Look for Plasmodium parasites.
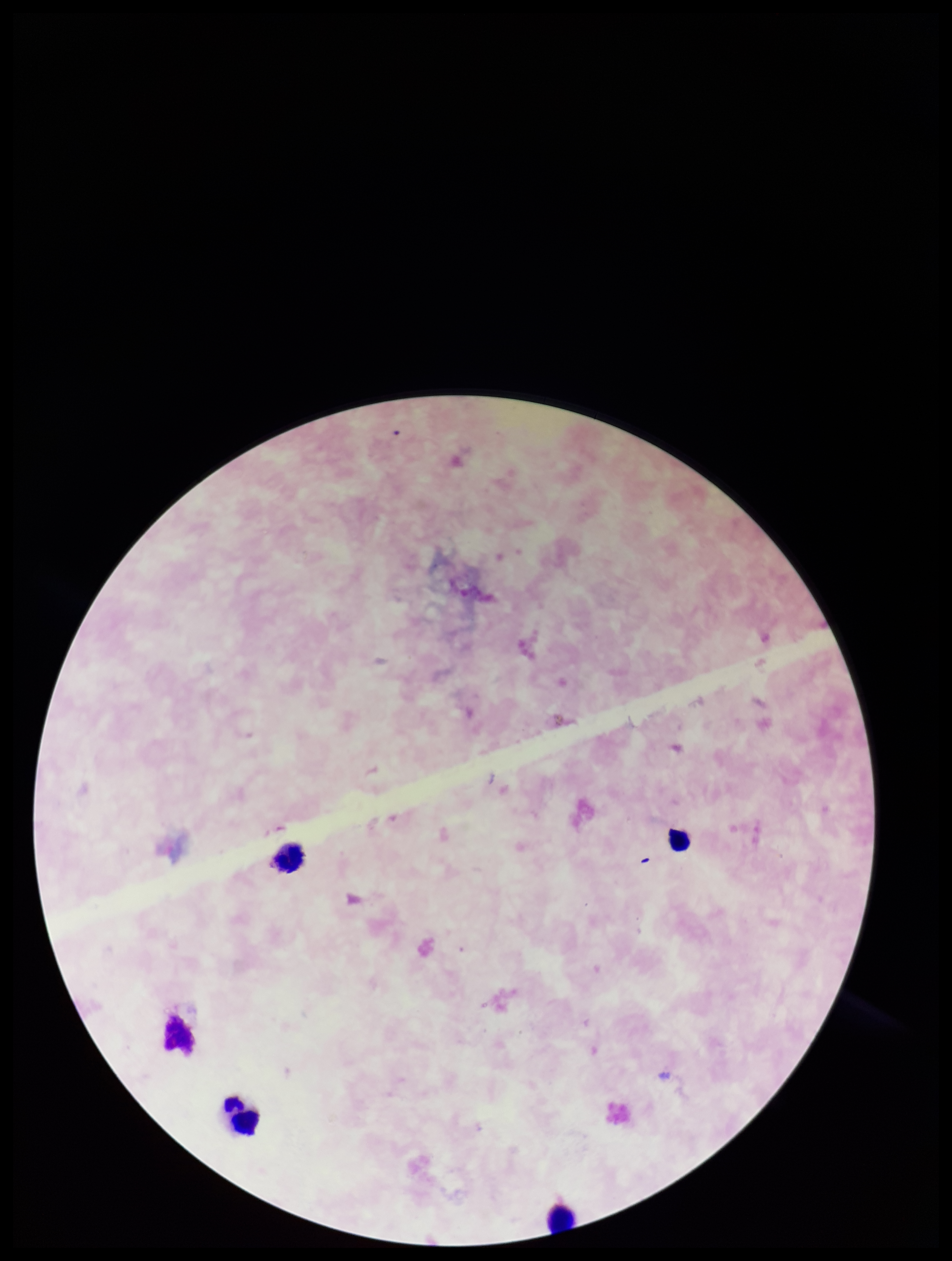

None identified.

parasite_count: 0
image_size: 952×1261 pixels
patient_malaria_status: negative
preparation: thick blood smear
capture: smartphone photograph through the microscope eyepiece
stain: Giemsa
field_of_view: single
leukocyte_count: 4